Assess the morphology of the erythrocytes.
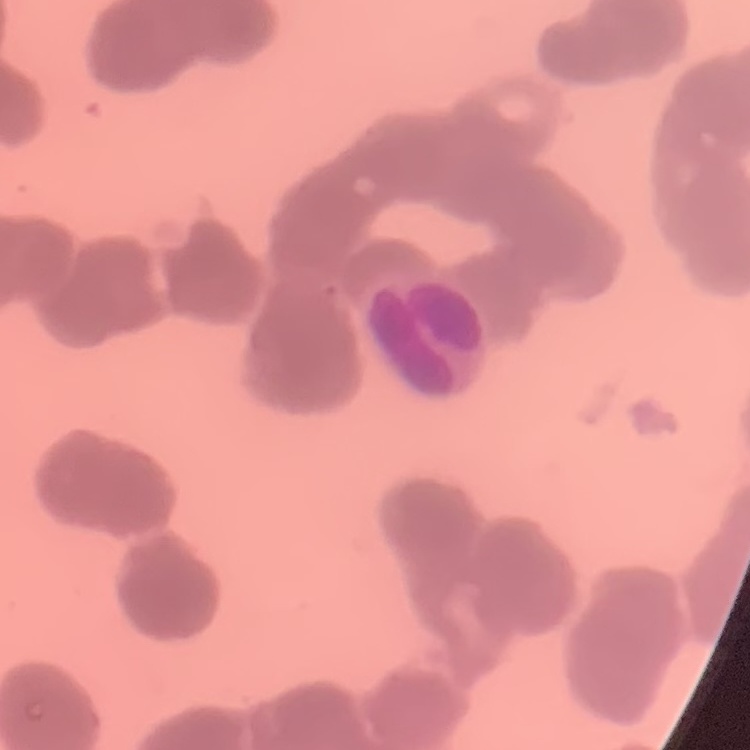

They show rouleaux formation.

Summary:
  - Preparation: thin peripheral smear
  - Stain: Field's or Giemsa
  - Image type: square crop of a larger photomicrograph